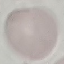 Malaria status: uninfected. Automatically extracted cell patch, resized to 64 × 64 pixels. Photographed with a smartphone camera at the microscope eyepiece. Thin smear of blood. Giemsa stain.